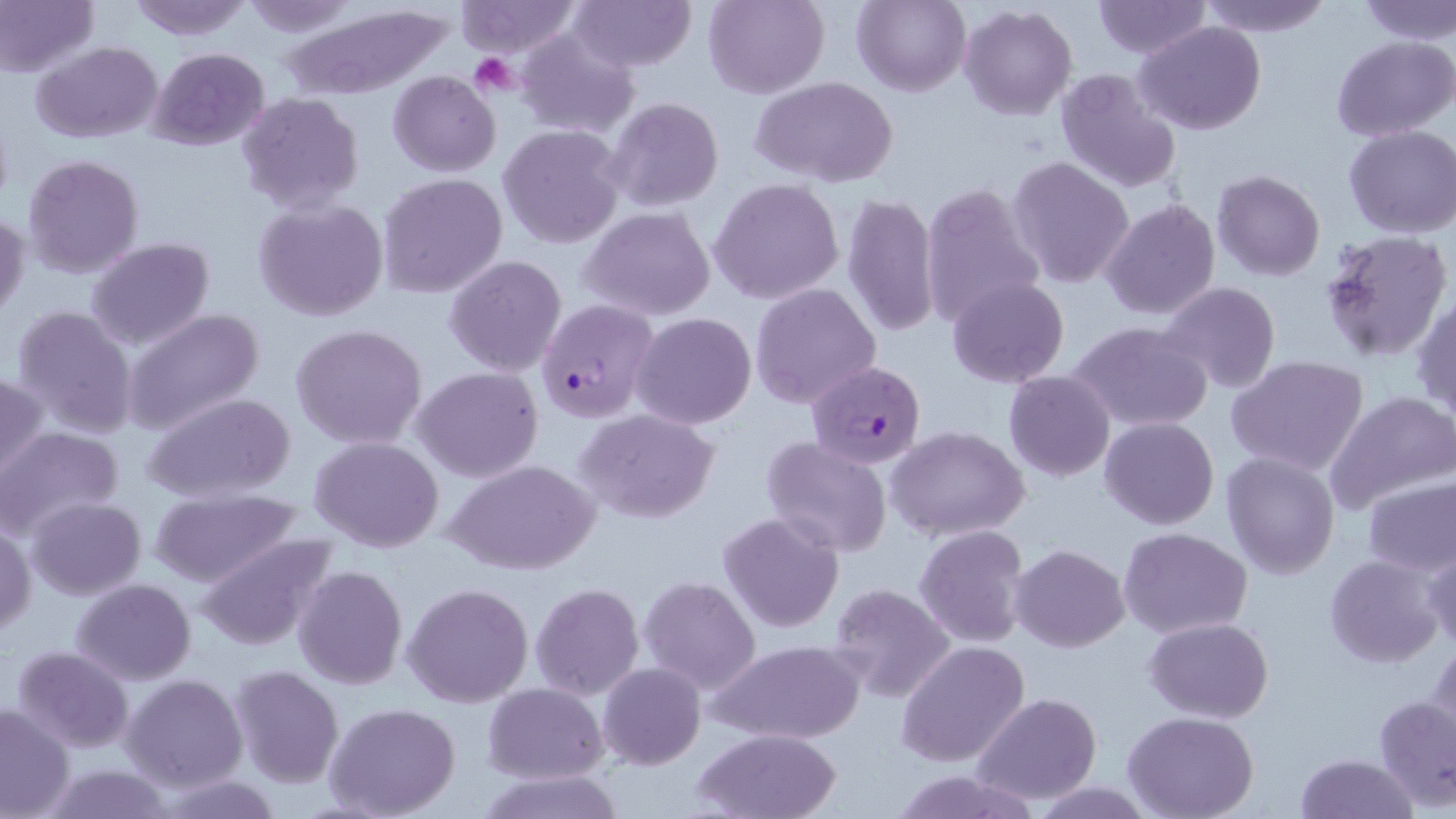
{
  "slide_level_diagnosis": "Plasmodium falciparum",
  "magnification": "1000x",
  "uninfected_red_blood_cell_locations": "approximate bounding boxes as (x1,y1)-(x2,y2) corner pairs in pixels: (124,0)-(253,41), (456,0)-(583,55), (568,0)-(694,72), (704,0)-(828,100), (853,0)-(969,98), (1197,0)-(1332,36), (1355,0)-(1456,42), (0,1)-(98,78), (240,1)-(356,36), (1093,1)-(1210,59), (278,2)-(462,102), (957,4)-(1078,121), (1134,22)-(1266,135), (514,30)-(640,138), (1331,34)-(1456,141), (32,41)-(163,144), (149,48)-(269,150), (388,69)-(500,177), (1054,70)-(1181,194), (753,76)-(897,188), (235,90)-(365,214), (604,97)-(725,213), (500,110)-(726,228), (499,124)-(624,250), (1342,125)-(1456,238), (22,154)-(144,278), (1006,154)-(1135,289), (1212,169)-(1325,280), (377,172)-(507,300), (709,177)-(844,304), (920,182)-(1047,328), (841,191)-(940,338), (253,197)-(388,322), (1099,197)-(1220,321), (577,206)-(717,322), (0,208)-(29,323), (1318,230)-(1452,365), (86,238)-(215,351), (444,255)-(567,377), (947,277)-(1069,388), (1158,281)-(1281,393), (750,283)-(881,410), (1412,295)-(1456,420), (10,304)-(138,439), (120,308)-(265,435), (630,312)-(757,429), (1068,320)-(1213,433), (290,324)-(428,451), (1226,355)-(1370,476), (413,367)-(543,483), (1003,370)-(1115,482), (0,371)-(48,483), (1325,391)-(1456,513), (143,393)-(296,503), (574,408)-(721,526), (1100,416)-(1218,530), (886,425)-(1031,542), (0,426)-(124,539), (761,435)-(892,557), (310,437)-(443,553), (1222,451)-(1340,578), (443,460)-(601,577), (1362,476)-(1456,577), (147,488)-(306,590), (26,497)-(146,599), (718,511)-(846,634), (1,522)-(36,637), (914,525)-(1029,648), (1120,527)-(1252,638), (193,532)-(339,649), (1010,543)-(1129,652), (1420,546)-(1456,651), (1324,555)-(1444,668), (293,564)-(407,691), (638,574)-(762,695), (71,578)-(196,684), (530,582)-(644,701), (830,582)-(958,705), (402,583)-(533,707), (88,590)-(216,748), (1145,617)-(1274,723), (1427,639)-(1455,750), (896,640)-(1030,768), (709,641)-(862,744), (10,644)-(137,752), (598,662)-(705,769), (229,664)-(344,788), (121,674)-(247,793), (483,683)-(607,783), (972,692)-(1101,804), (1373,696)-(1455,810), (0,702)-(75,818), (324,702)-(462,819), (1122,712)-(1260,819), (693,730)-(841,818), (1294,752)-(1420,819), (38,764)-(177,819), (475,769)-(625,819), (153,773)-(287,818)",
  "preparation": "thin blood smear",
  "field_of_view": "single",
  "platelet_locations": "approximate bounding boxes as (x1,y1)-(x2,y2) corner pairs in pixels: (473,55)-(521,97)",
  "image_size": "1456×819 pixels",
  "plasmodium_falciparum_infected_red_blood_cell_locations": "approximate bounding boxes as (x1,y1)-(x2,y2) corner pairs in pixels: (537,301)-(658,423), (809,360)-(926,469)",
  "modality": "optical microscopy",
  "stain": "May-Grünwald-Giemsa"
}